Describe the morphology of the erythrocytes.
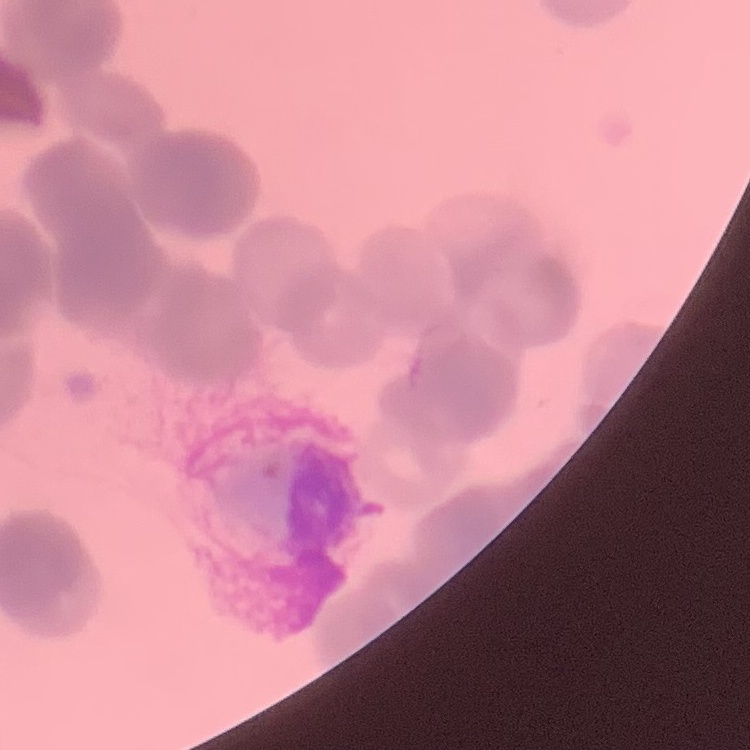

Rouleaux formation.

One tile cut from a larger photomicrograph. Stained with either Field's or Giemsa. Thin peripheral smear.